State the preparation type.
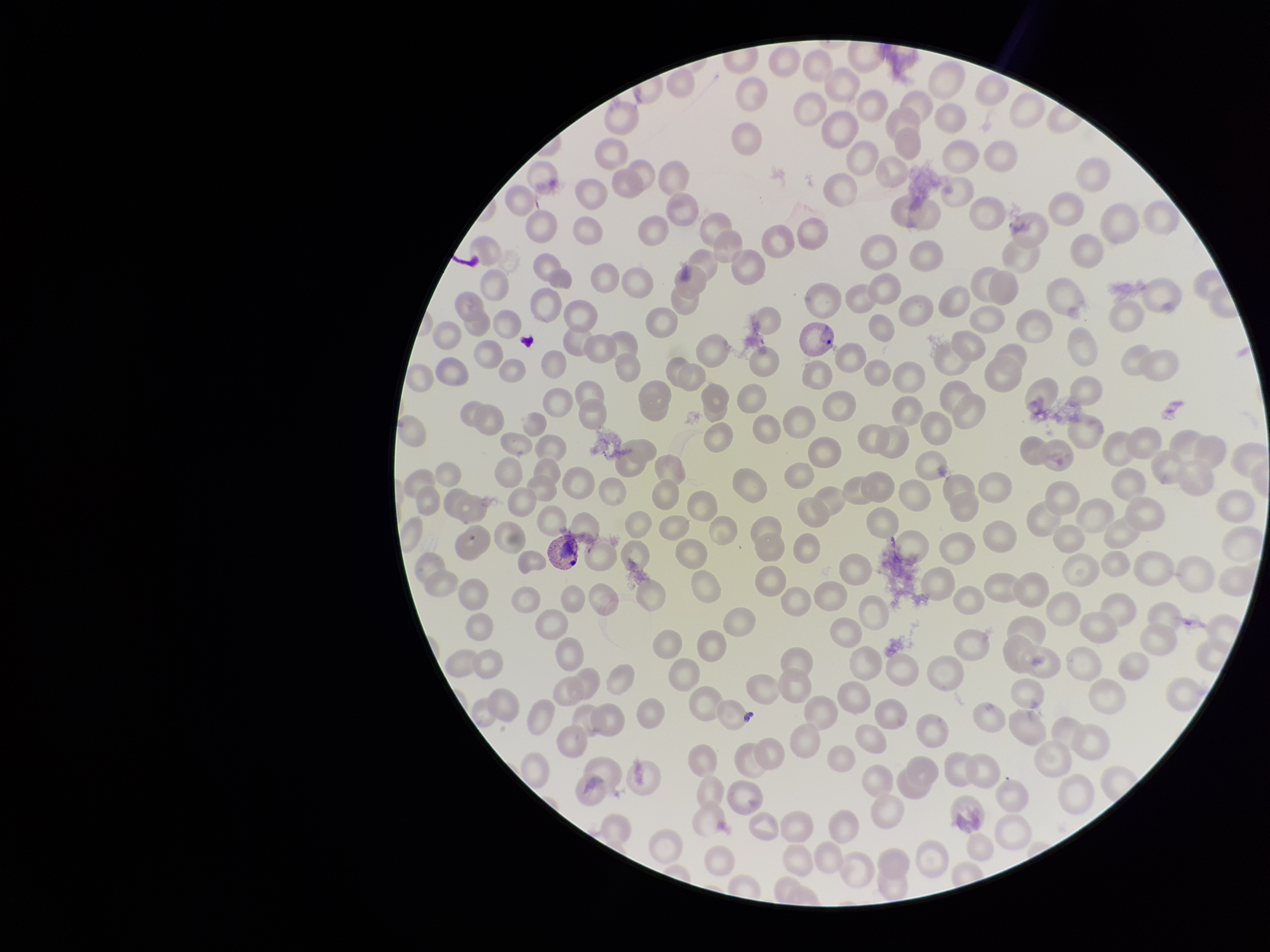

Thin.

image size = 1270×952 pixels
stain = Giemsa
parasitized red blood cell count = 1
red blood cell count = 229
field of view = one from this slide
patient malaria status = infected
parasitized red blood cells = identified
capture = smartphone photograph through the microscope eyepiece
species reported for this patient = Plasmodium vivax